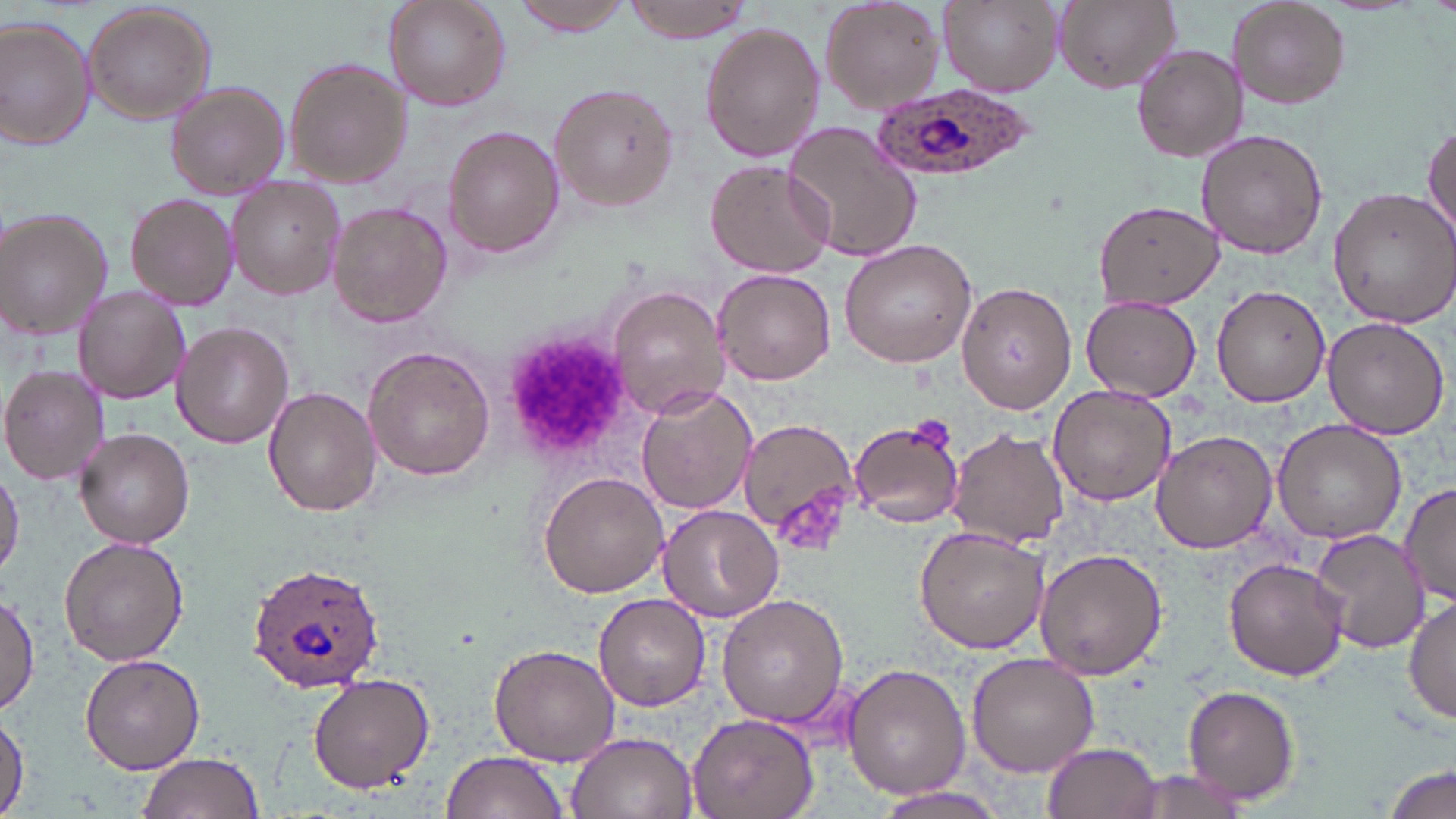
Approximate bounding boxes as [x1, y1, x2, y2] in pixels. Platelet locations: [502, 332, 634, 461], [909, 416, 952, 454], [772, 482, 848, 555]. Uninfected red blood cell locations: [383, 0, 510, 110], [819, 0, 945, 114], [939, 0, 1063, 94], [1050, 0, 1179, 94], [1228, 0, 1349, 109], [510, 1, 635, 36], [620, 1, 759, 40], [82, 2, 217, 124], [0, 18, 96, 150], [701, 22, 826, 163], [1131, 44, 1247, 163], [283, 57, 411, 190], [550, 81, 679, 211], [168, 82, 290, 199], [782, 119, 923, 264], [1423, 121, 1456, 240], [444, 126, 564, 258], [1196, 128, 1327, 260], [706, 161, 834, 277], [227, 175, 345, 300], [1326, 187, 1456, 328], [128, 192, 240, 312], [1093, 199, 1223, 308], [328, 201, 452, 327], [0, 208, 115, 341], [838, 239, 979, 370], [713, 268, 836, 385], [957, 281, 1076, 413], [607, 284, 730, 419], [75, 286, 189, 403], [1211, 286, 1331, 407], [1082, 295, 1201, 400], [1322, 317, 1450, 438], [171, 321, 293, 449], [363, 346, 495, 481], [1, 364, 111, 486], [1046, 384, 1176, 506], [636, 386, 756, 514], [265, 387, 380, 516], [850, 417, 966, 529], [735, 418, 863, 541], [1271, 418, 1408, 543], [74, 427, 195, 548], [946, 427, 1068, 550], [1150, 428, 1276, 552], [1, 467, 24, 579], [538, 472, 668, 599], [1398, 481, 1456, 609], [658, 504, 782, 621], [915, 526, 1049, 652], [1312, 529, 1429, 652], [58, 537, 188, 664], [1033, 548, 1170, 682], [1225, 558, 1348, 680], [717, 593, 849, 728], [0, 594, 39, 712], [593, 594, 710, 711], [1405, 595, 1456, 729], [489, 644, 623, 767], [79, 651, 204, 773], [966, 653, 1099, 778], [841, 663, 969, 797], [308, 671, 436, 791], [1180, 685, 1301, 806], [687, 712, 819, 819], [0, 715, 26, 813], [567, 731, 696, 819], [1043, 741, 1161, 819], [440, 750, 569, 819], [135, 752, 263, 819], [1384, 761, 1455, 819], [1114, 767, 1260, 819], [869, 785, 1012, 817]. Plasmodium ovale-infected red blood cell locations: [872, 82, 1036, 187], [248, 561, 388, 692]. Slide-level diagnosis: Plasmodium ovale. Image is 1456×819 pixels. Thin blood smear. 1000x magnification. Light microscopy. May-Grünwald-Giemsa-stained preparation. Single field of view.